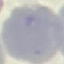

Malaria status: uninfected. Thin smear of blood. Giemsa stain. Photographed with a smartphone camera at the microscope eyepiece. Cell patch, automatically extracted from a larger field of view and resized to 64 × 64 pixels.